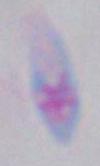 Toxoplasma gondii is shown. Photomicrograph. Captured at 1000x magnification.